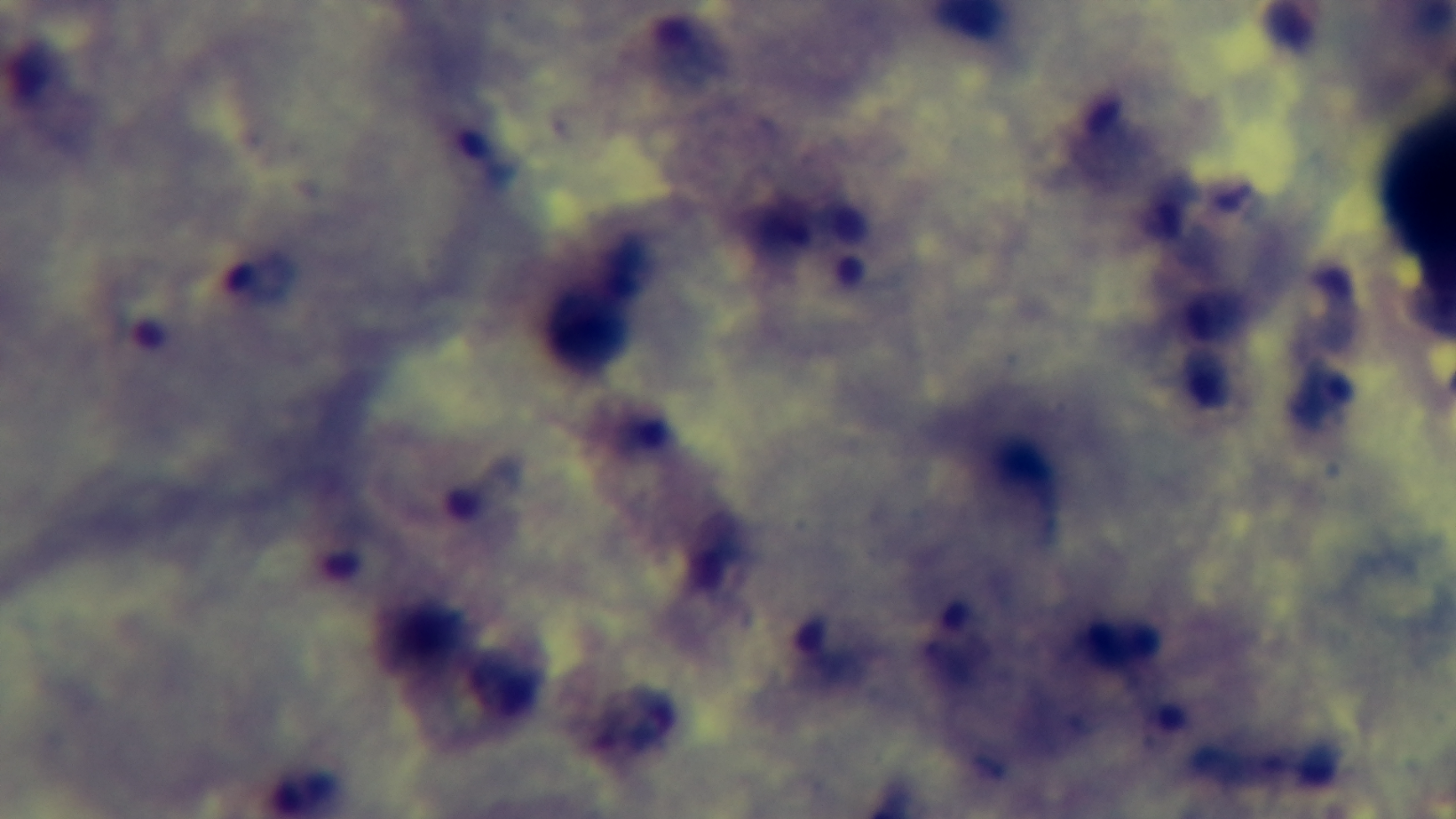
Summary:
  - Objective: 100x oil immersion
  - Capture: mounted 4K digital camera
  - Stain: Giemsa
  - Malaria status: positive
  - Preparation: thick smear
  - Field of view: single
  - Modality: light microscopy